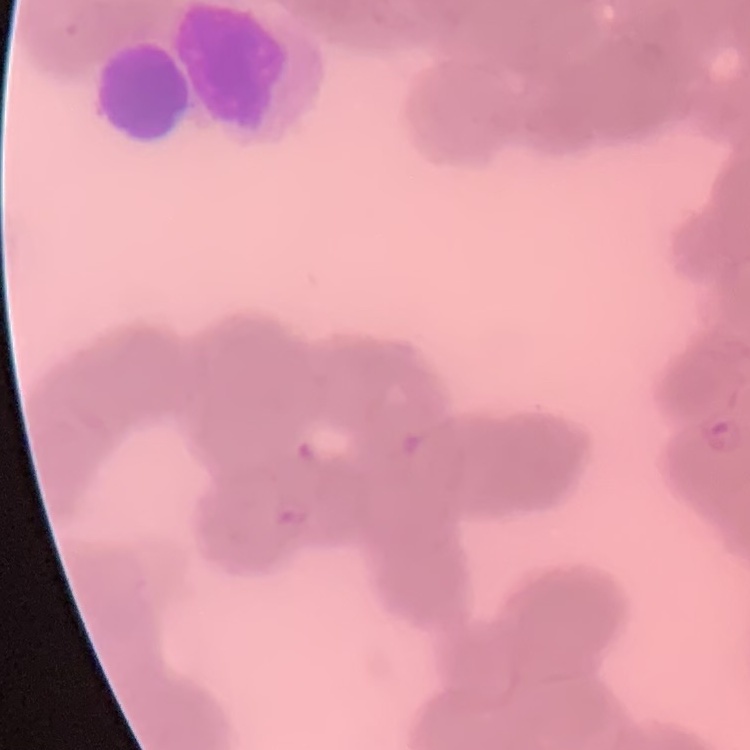
Summary:
  - Red blood cell morphology: rouleaux formation
  - Image type: square crop of a larger photomicrograph
  - Preparation: thin blood film
  - Stain: Field's or Giemsa